Report the malaria status of this cell.
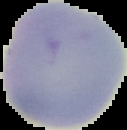
Uninfected.

Summary:
  - Image size: 127×130 pixels
  - Preparation: thin blood film
  - Image type: cell region segmented out of the field of view; surrounding area masked to black